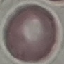
Malaria status: uninfected. Photographed with a smartphone camera at the microscope eyepiece. Giemsa stain. Thin blood film. Automatically extracted cell patch, resized to 64 × 64 pixels.